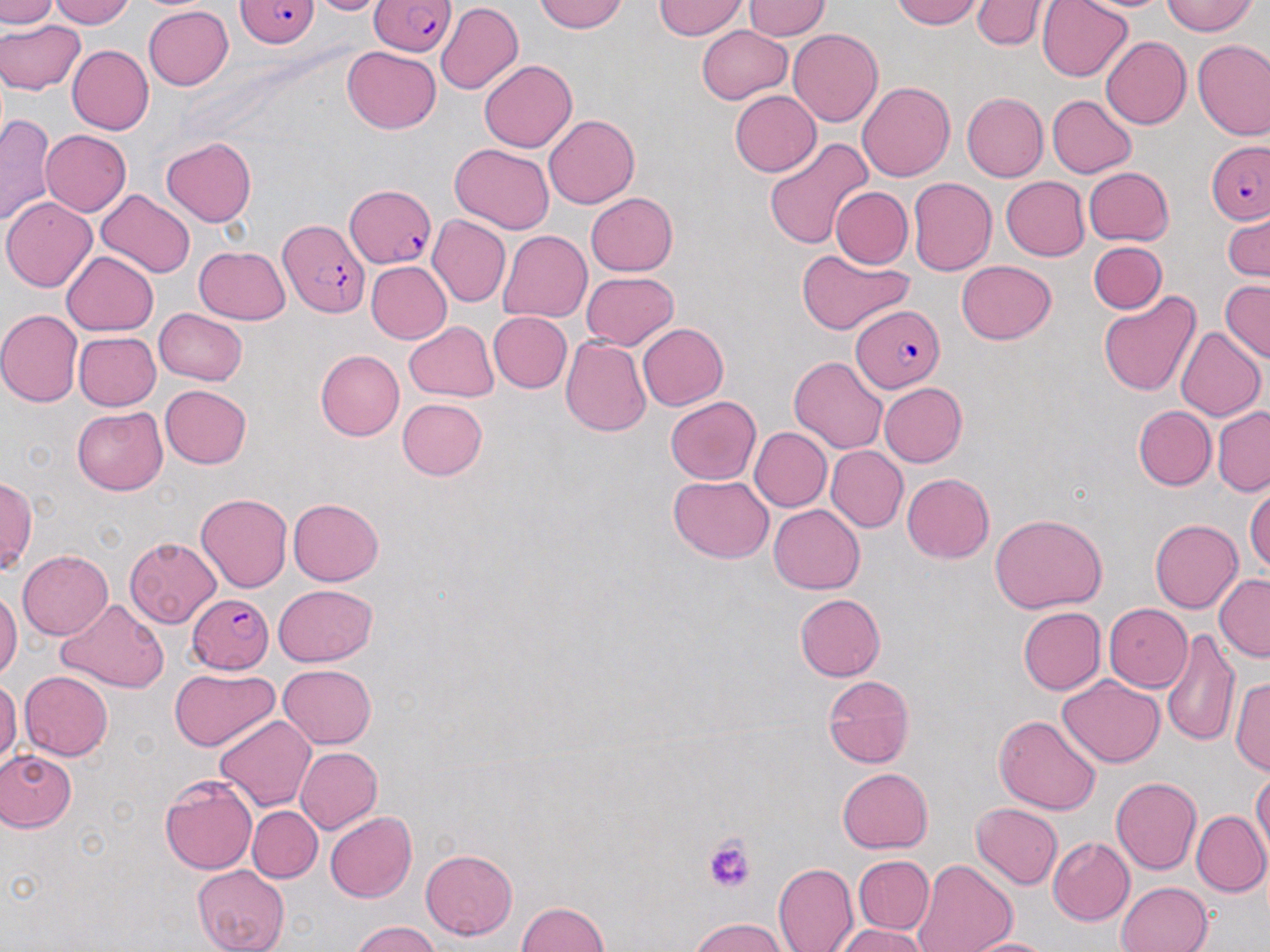 Approximate bounding boxes as (x1, y1, x2, y2) in pixels. Uninfected red blood cell locations: (0, 0, 57, 28), (48, 0, 134, 27), (304, 0, 395, 15), (534, 0, 629, 33), (891, 0, 984, 29), (973, 0, 1047, 50), (1037, 0, 1132, 82), (1072, 0, 1176, 12), (1162, 0, 1258, 36), (655, 1, 750, 39), (740, 2, 832, 40), (436, 3, 523, 95), (143, 6, 233, 89), (0, 21, 85, 94), (697, 25, 792, 103), (788, 28, 882, 127), (1102, 37, 1191, 129), (1193, 39, 1270, 140), (67, 45, 155, 135), (342, 46, 440, 133), (479, 60, 577, 152), (857, 81, 955, 182), (730, 90, 820, 176), (961, 93, 1048, 182), (1047, 95, 1136, 177), (0, 113, 56, 226), (544, 114, 639, 210), (40, 129, 131, 216), (763, 137, 875, 251), (161, 138, 257, 226), (451, 144, 554, 232), (1083, 167, 1174, 246), (1001, 176, 1089, 261), (908, 177, 998, 276), (830, 187, 912, 268), (96, 190, 195, 278), (585, 192, 677, 276), (2, 196, 97, 291), (1224, 209, 1269, 283), (427, 215, 511, 307), (498, 231, 592, 323), (1089, 242, 1166, 314), (195, 245, 290, 324), (797, 247, 912, 336), (61, 250, 158, 335), (956, 261, 1056, 344), (367, 262, 451, 344), (581, 271, 679, 350), (1220, 279, 1270, 363), (1098, 291, 1202, 398), (154, 308, 247, 385), (0, 309, 83, 407), (488, 311, 572, 392), (404, 321, 498, 401), (638, 323, 728, 409), (1174, 326, 1266, 421), (73, 331, 161, 411), (561, 335, 652, 437), (316, 349, 404, 441), (789, 356, 887, 454), (879, 382, 967, 467), (160, 384, 252, 469), (664, 396, 761, 484), (397, 398, 488, 480), (72, 405, 168, 495), (1132, 405, 1215, 491), (1212, 405, 1270, 497), (750, 427, 831, 512), (826, 446, 907, 532), (902, 473, 994, 564), (669, 475, 774, 563), (1, 476, 35, 573), (1246, 484, 1270, 574), (195, 493, 292, 593), (288, 498, 383, 585), (768, 504, 864, 594), (990, 515, 1109, 615), (1149, 519, 1242, 613), (124, 537, 221, 628), (18, 550, 113, 639), (1214, 573, 1270, 661), (273, 584, 377, 666), (0, 589, 22, 679), (795, 593, 885, 681), (58, 598, 167, 692), (1104, 604, 1192, 690), (1018, 606, 1106, 694), (1161, 628, 1242, 747), (278, 664, 377, 748), (170, 667, 280, 752), (19, 671, 113, 760), (822, 674, 915, 769), (1058, 676, 1165, 767), (1230, 676, 1270, 774), (0, 677, 21, 767), (993, 714, 1101, 815), (214, 716, 316, 811), (295, 747, 382, 833), (0, 750, 76, 831), (837, 767, 933, 852), (1251, 769, 1270, 863), (160, 775, 258, 874), (1110, 776, 1201, 874), (971, 803, 1062, 889), (248, 807, 322, 883), (325, 811, 416, 903), (1191, 811, 1270, 897), (1047, 837, 1134, 926), (421, 848, 517, 939), (853, 854, 933, 934), (914, 859, 1017, 952), (772, 862, 858, 952), (192, 866, 290, 952), (1116, 881, 1213, 952), (518, 901, 609, 951), (688, 917, 788, 951), (352, 921, 438, 952), (835, 924, 928, 952), (958, 937, 1058, 952). Plasmodium falciparum-infected red blood cell locations: (235, 0, 321, 48), (372, 0, 457, 56), (1207, 140, 1270, 222), (346, 185, 437, 269), (279, 219, 370, 317), (853, 303, 946, 394), (187, 596, 274, 675). Platelet locations: (705, 835, 755, 894). Slide-level diagnosis: Plasmodium falciparum. Thin blood smear. Single field of view. Image is 1270×952 pixels. Captured at 1000x magnification. Light microscopy. May-Grünwald-Giemsa-stained preparation.